Describe the morphology of the red blood cells.
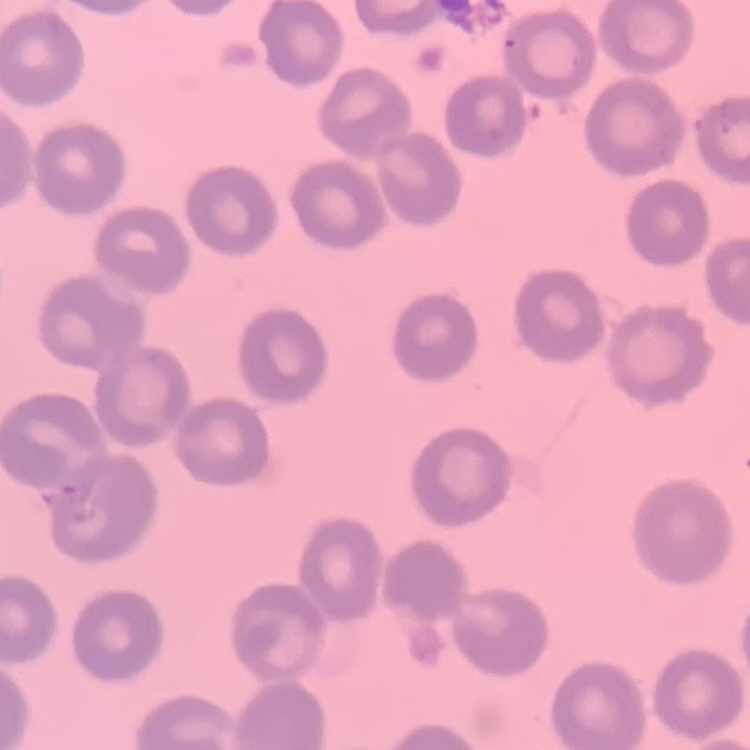

No rouleaux formation.

Thin peripheral smear. Square crop of a larger photomicrograph. Field's or Giemsa stain.